Look for parasitized red blood cells.
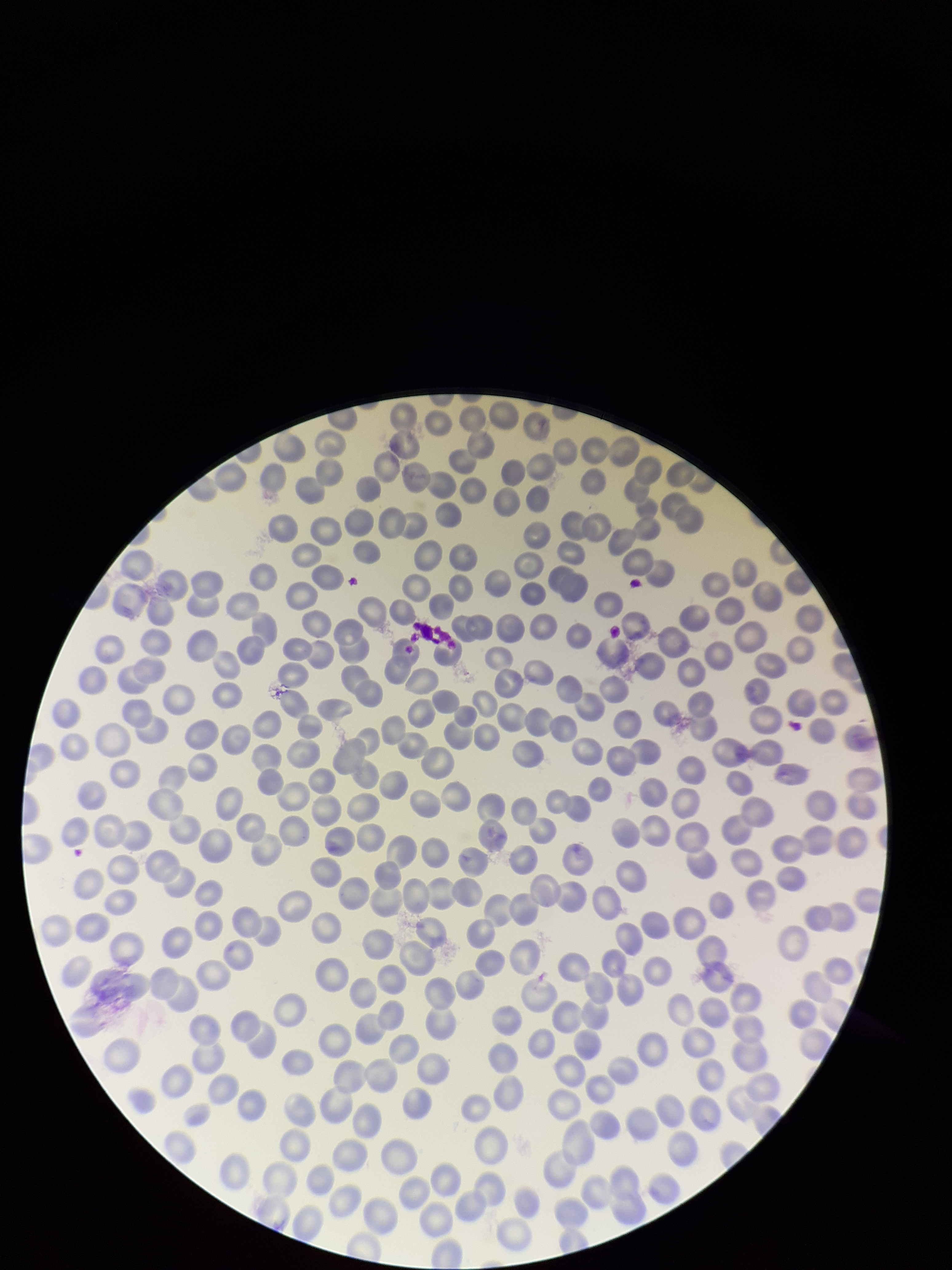
None detected.

Giemsa stain. Smartphone photograph taken through the eyepiece of a microscope. Single field of view. Image is 952×1270 pixels. Parasitized red blood cell count: 0. Preparation: thin blood smear. Red blood cell count: 274. Patient malaria status: negative.